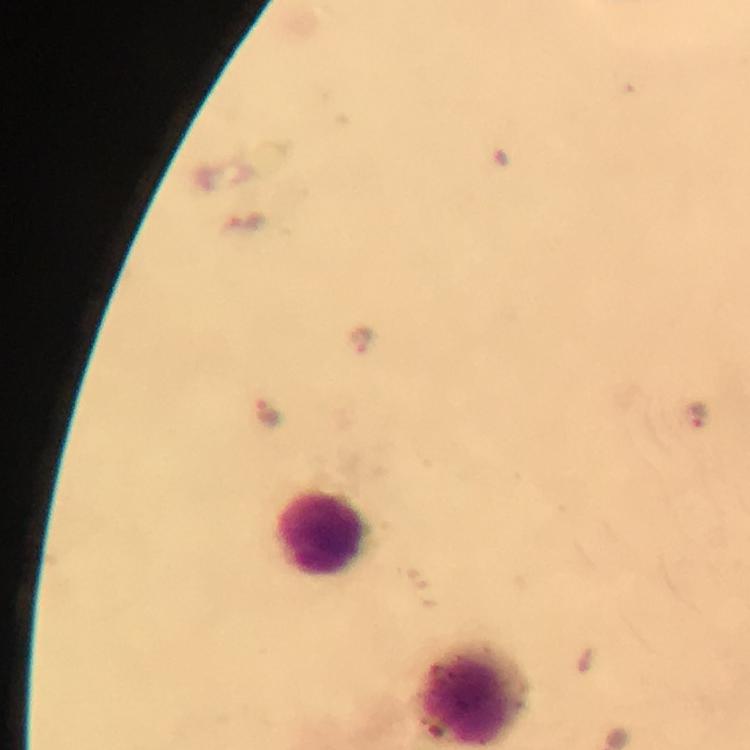

leukocyte locations = approximate centers as {x, y} in pixels: {320, 533}, {468, 696}
capture = smartphone photograph through a microscope
preparation = thick blood smear
Plasmodium parasite locations = approximate centers as {x, y} in pixels: {360, 342}, {271, 412}, {692, 413}
immersion oil = used
context = from a malaria diagnostic workup
cropped from = one field of view
stain = Giemsa
magnification = 100x
image size = 750×750 pixels